Outline each blood parasite and name the species.
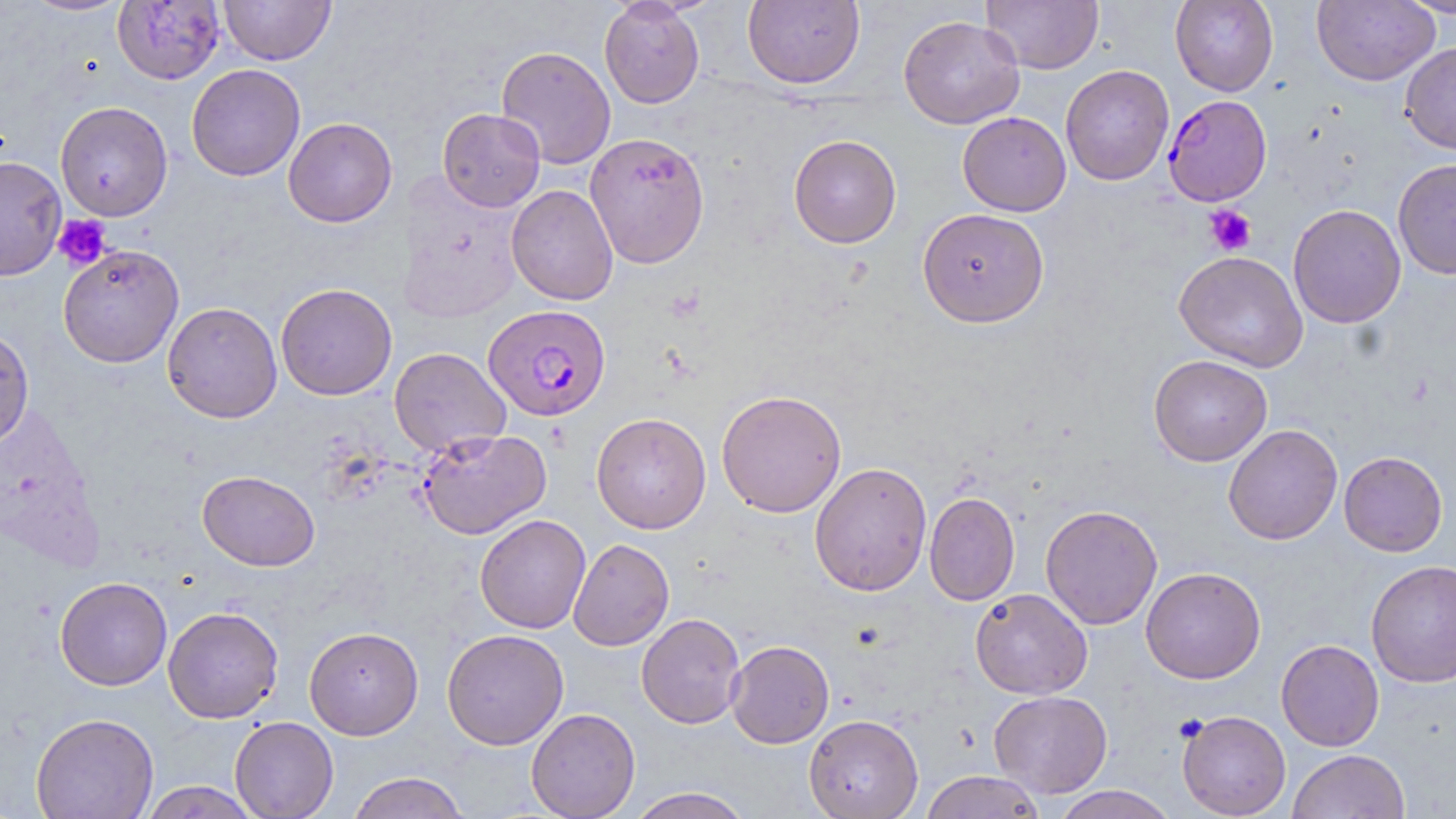

Approximate bounding boxes as (x1,y1)-(x2,y2) corner pairs in pixels.
Plasmodium falciparum-infected red blood cells: (1163,94)-(1272,206), (484,304)-(611,422).
No Plasmodium ovale, Plasmodium malariae, Plasmodium vivax, Babesia divergens, or Trypanosoma brucei observed.

Summary:
  - Uninfected red blood cell locations: (20,0)-(134,17), (112,0)-(225,85), (219,0)-(336,65), (599,0)-(705,109), (982,0)-(1103,74), (1170,0)-(1278,96), (1312,0)-(1439,86), (1398,0)-(1456,19), (742,1)-(865,89), (898,15)-(1025,129), (1400,42)-(1456,155), (496,45)-(616,169), (186,64)-(305,181), (1060,65)-(1175,186), (55,101)-(173,221), (437,108)-(545,212), (957,111)-(1071,216), (283,117)-(397,227), (584,132)-(710,267), (788,134)-(902,248), (0,156)-(67,281), (1392,158)-(1456,280), (506,184)-(618,305), (1288,203)-(1406,328), (917,207)-(1049,327), (58,245)-(184,368), (1174,251)-(1308,372), (276,283)-(397,400), (162,301)-(283,423), (0,327)-(35,448), (389,347)-(510,457), (1149,354)-(1272,466), (716,389)-(847,518), (591,412)-(711,534), (1223,424)-(1343,545), (416,428)-(552,540), (1338,451)-(1448,556), (809,461)-(932,597), (197,470)-(320,571), (924,491)-(1020,606), (1040,504)-(1163,630), (474,514)-(591,634), (568,538)-(675,651), (1366,559)-(1456,687), (1141,567)-(1265,684), (55,576)-(172,690), (970,588)-(1092,699), (162,606)-(284,724), (636,613)-(746,729), (304,626)-(423,739), (442,629)-(568,750), (1276,639)-(1384,751), (726,640)-(834,749), (988,690)-(1113,798), (526,707)-(641,819), (1177,709)-(1291,818), (30,712)-(159,819), (804,713)-(923,819), (230,716)-(338,819), (1288,749)-(1410,819), (920,770)-(1047,819), (346,771)-(471,819), (139,781)-(261,818), (1051,785)-(1179,819), (627,787)-(752,818)
  - Platelet locations: (1204,205)-(1256,256), (52,214)-(112,271)
  - Slide-level diagnosis: Plasmodium falciparum
  - Stain: May-Grünwald-Giemsa
  - Modality: optical microscopy
  - Magnification: 1000x
  - Field of view: single
  - Image size: 1456×819 pixels
  - Preparation: thin blood smear